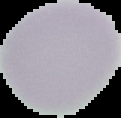 Cell region segmented out of the field of view; the surrounding area is masked to black. From a thin blood smear. Malaria status: uninfected. Image is 121×118 pixels.